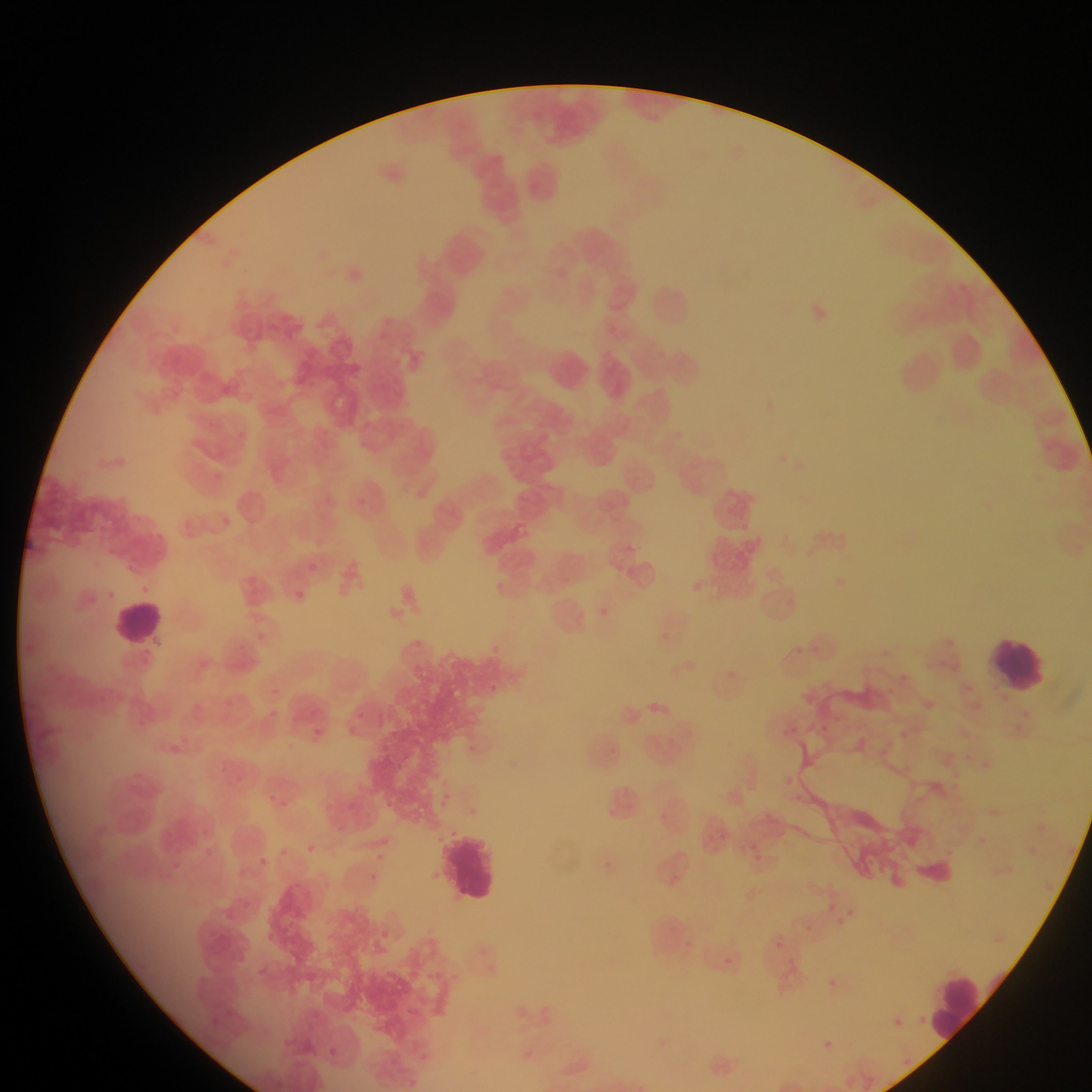
{
  "malaria_parasite_locations": "approximate bounding boxes as [left, top, right, bottom] in pixels: [287, 585, 310, 606], [716, 663, 742, 688], [959, 680, 977, 698], [644, 694, 676, 725], [159, 736, 191, 767], [1031, 818, 1052, 839], [971, 832, 990, 849], [302, 841, 319, 857], [742, 841, 769, 868], [275, 843, 291, 859], [369, 848, 394, 870], [372, 850, 387, 864], [252, 852, 273, 872], [590, 853, 623, 882], [364, 870, 382, 886], [822, 898, 839, 914], [829, 905, 859, 931], [771, 935, 789, 952], [718, 951, 739, 972], [779, 956, 799, 978], [818, 973, 843, 998], [885, 1012, 907, 1033], [815, 1033, 839, 1056], [322, 1045, 341, 1062]",
  "country": "Ghana",
  "capture": "mobile-phone photograph through a microscope",
  "leukocyte_locations": "approximate bounding boxes as [left, top, right, bottom] in pixels: [520, 157, 567, 205], [644, 279, 698, 333], [544, 347, 598, 401], [592, 354, 640, 403], [108, 598, 165, 648], [986, 634, 1053, 696], [439, 826, 505, 910], [930, 973, 990, 1039]",
  "field_of_view": "single",
  "preparation": "thin blood smear",
  "image_size": "1092×1092 pixels"
}